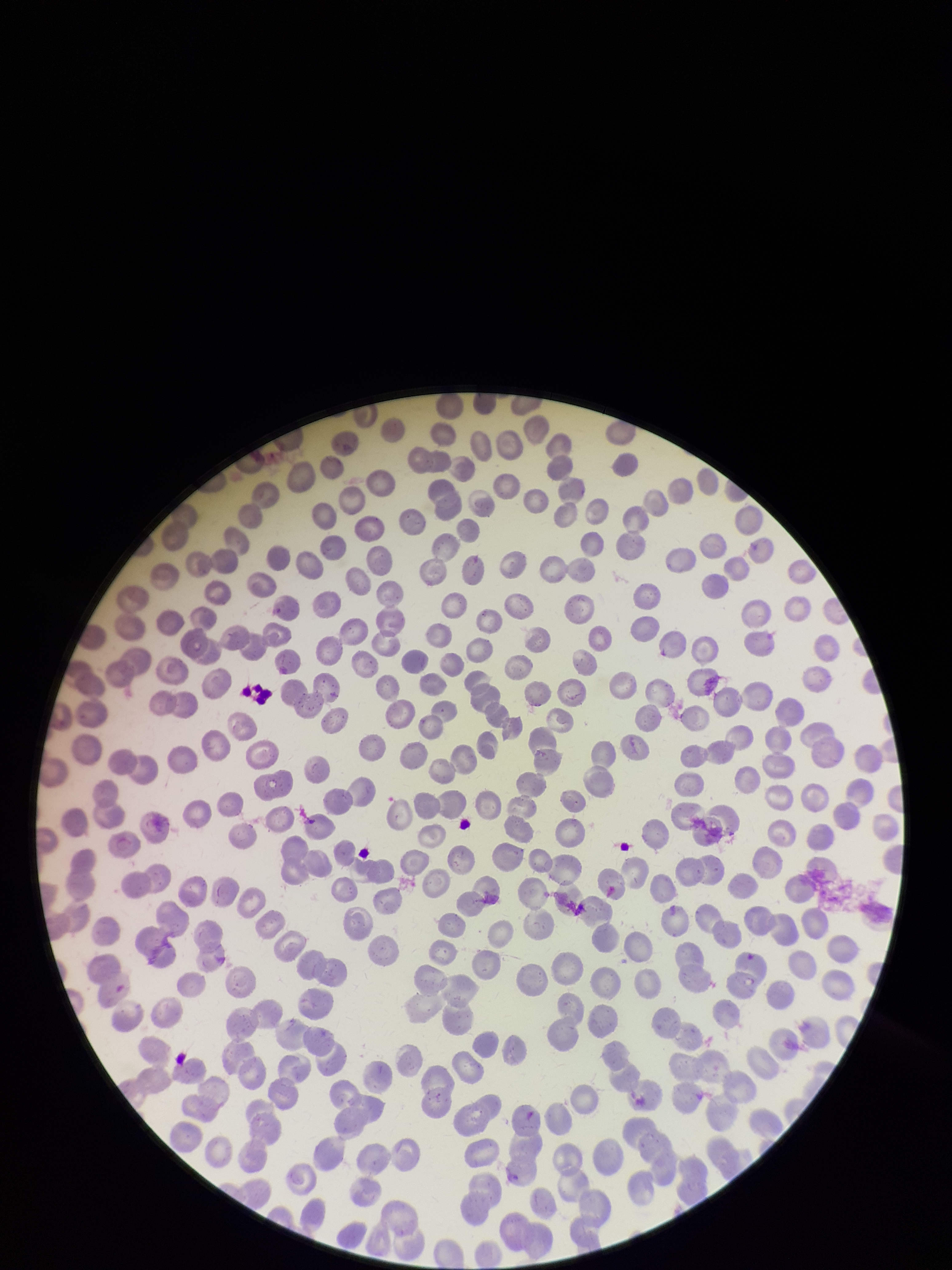
field_of_view: one from this slide
parasitized_red_blood_cells: none detected
patient_malaria_status: negative
parasitized_red_blood_cell_count: 0
preparation: thin
image_size: 952×1270 pixels
red_blood_cell_count: 346
capture: smartphone photograph through the microscope eyepiece
stain: Giemsa